State which parasite is depicted.
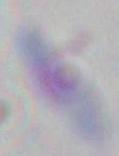

This is Toxoplasma gondii.

Micrograph. Captured at 1000x magnification.